Locate every Plasmodium falciparum-infected red blood cell.
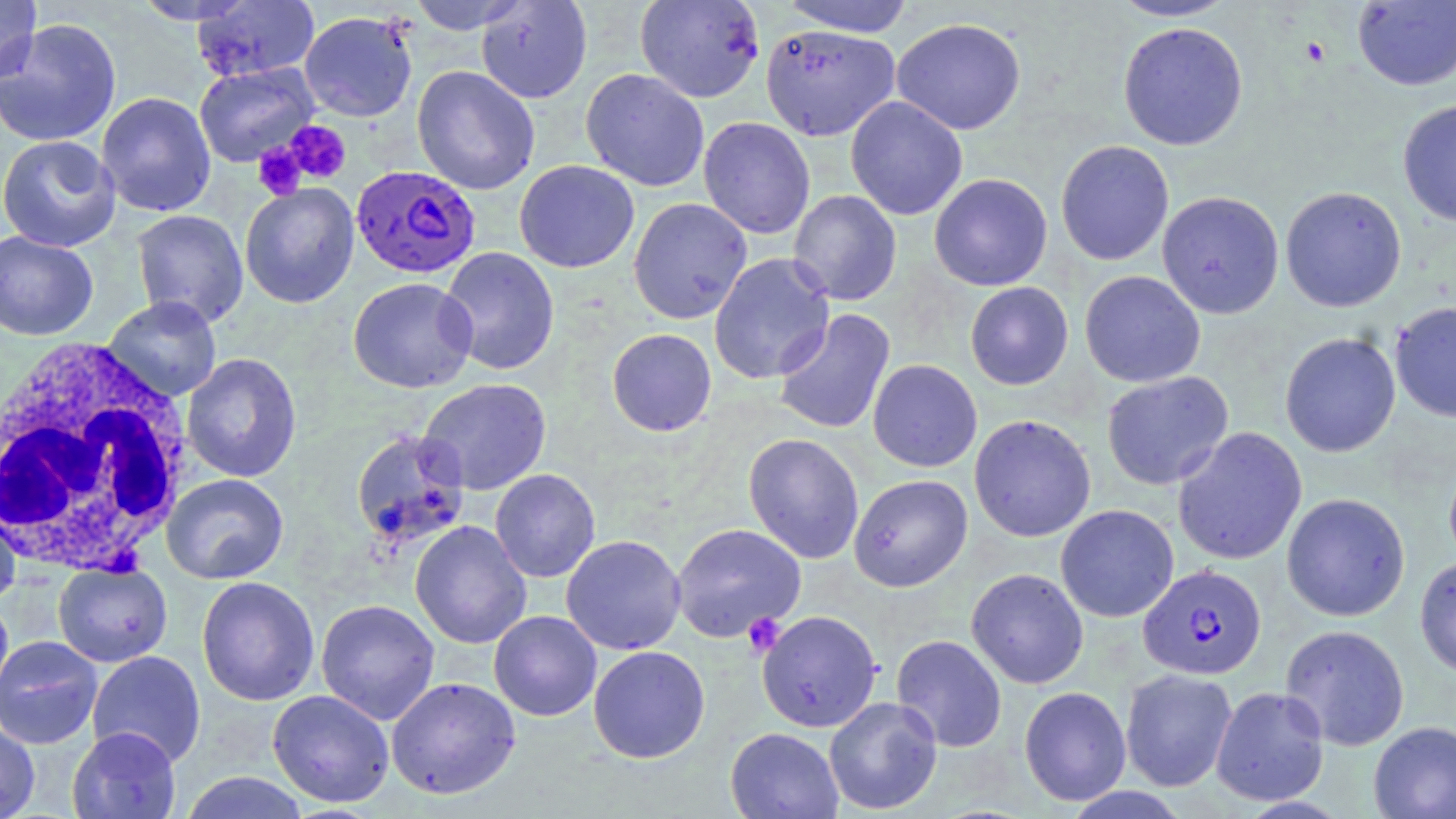

Approximate bounding boxes as named x1/y1/x2/y2 corners in pixels.
Plasmodium falciparum-infected red blood cells: (x1=351, y1=165, x2=481, y2=279), (x1=1138, y1=563, x2=1266, y2=680).

Summary:
  - White blood cell locations: (x1=0, y1=339, x2=196, y2=577)
  - Uninfected red blood cell locations: (x1=130, y1=0, x2=258, y2=25), (x1=405, y1=0, x2=533, y2=34), (x1=635, y1=0, x2=765, y2=103), (x1=778, y1=0, x2=915, y2=37), (x1=1108, y1=0, x2=1238, y2=21), (x1=0, y1=1, x2=42, y2=84), (x1=190, y1=1, x2=320, y2=83), (x1=475, y1=1, x2=593, y2=103), (x1=1352, y1=1, x2=1456, y2=91), (x1=299, y1=10, x2=418, y2=122), (x1=891, y1=17, x2=1026, y2=135), (x1=0, y1=18, x2=122, y2=148), (x1=1118, y1=22, x2=1248, y2=150), (x1=760, y1=24, x2=901, y2=141), (x1=194, y1=62, x2=318, y2=167), (x1=411, y1=65, x2=540, y2=195), (x1=581, y1=68, x2=709, y2=192), (x1=96, y1=92, x2=216, y2=217), (x1=845, y1=96, x2=967, y2=220), (x1=1397, y1=99, x2=1456, y2=227), (x1=698, y1=116, x2=815, y2=239), (x1=0, y1=135, x2=121, y2=252), (x1=1055, y1=140, x2=1174, y2=265), (x1=514, y1=160, x2=639, y2=273), (x1=929, y1=173, x2=1052, y2=291), (x1=240, y1=183, x2=359, y2=308), (x1=1280, y1=186, x2=1406, y2=312), (x1=788, y1=190, x2=902, y2=305), (x1=1157, y1=190, x2=1284, y2=319), (x1=628, y1=197, x2=752, y2=324), (x1=130, y1=209, x2=248, y2=328), (x1=0, y1=230, x2=99, y2=341), (x1=438, y1=247, x2=560, y2=376), (x1=709, y1=253, x2=836, y2=384), (x1=1079, y1=270, x2=1206, y2=388), (x1=348, y1=277, x2=477, y2=393), (x1=965, y1=281, x2=1074, y2=390), (x1=101, y1=296, x2=223, y2=402), (x1=1389, y1=301, x2=1456, y2=423), (x1=773, y1=308, x2=895, y2=435), (x1=606, y1=328, x2=717, y2=436), (x1=1280, y1=332, x2=1401, y2=457), (x1=181, y1=353, x2=302, y2=483), (x1=868, y1=359, x2=982, y2=472), (x1=1101, y1=371, x2=1234, y2=490), (x1=417, y1=378, x2=552, y2=495), (x1=969, y1=414, x2=1096, y2=542), (x1=1172, y1=427, x2=1307, y2=565), (x1=349, y1=428, x2=470, y2=551), (x1=743, y1=433, x2=865, y2=564), (x1=1444, y1=453, x2=1456, y2=571), (x1=490, y1=469, x2=601, y2=582), (x1=161, y1=474, x2=289, y2=584), (x1=849, y1=474, x2=972, y2=591), (x1=1281, y1=492, x2=1410, y2=621), (x1=0, y1=502, x2=20, y2=610), (x1=1055, y1=504, x2=1179, y2=622), (x1=410, y1=521, x2=531, y2=649), (x1=671, y1=523, x2=806, y2=642), (x1=561, y1=534, x2=686, y2=655), (x1=1414, y1=555, x2=1456, y2=679), (x1=53, y1=562, x2=173, y2=667), (x1=966, y1=568, x2=1088, y2=689), (x1=196, y1=576, x2=320, y2=706), (x1=0, y1=593, x2=14, y2=710), (x1=315, y1=599, x2=440, y2=725), (x1=488, y1=610, x2=602, y2=721), (x1=756, y1=610, x2=882, y2=732), (x1=1280, y1=624, x2=1410, y2=750), (x1=891, y1=634, x2=1007, y2=752), (x1=0, y1=635, x2=104, y2=749), (x1=588, y1=645, x2=710, y2=763), (x1=86, y1=650, x2=206, y2=767), (x1=1120, y1=668, x2=1237, y2=792), (x1=386, y1=676, x2=520, y2=799), (x1=1019, y1=686, x2=1132, y2=806), (x1=1210, y1=686, x2=1330, y2=806), (x1=267, y1=689, x2=394, y2=808), (x1=824, y1=696, x2=943, y2=815), (x1=0, y1=718, x2=40, y2=819), (x1=1368, y1=720, x2=1456, y2=819), (x1=67, y1=726, x2=181, y2=819), (x1=725, y1=727, x2=844, y2=818), (x1=178, y1=772, x2=311, y2=819)
  - Platelet locations: (x1=1300, y1=36, x2=1330, y2=67), (x1=284, y1=120, x2=351, y2=183), (x1=253, y1=144, x2=307, y2=200), (x1=742, y1=613, x2=787, y2=658)
  - Slide-level diagnosis: Plasmodium falciparum
  - Image size: 1456×819 pixels
  - Field of view: single
  - Modality: light microscopy
  - Magnification: 1000x
  - Preparation: thin blood smear
  - Stain: May-Grünwald-Giemsa